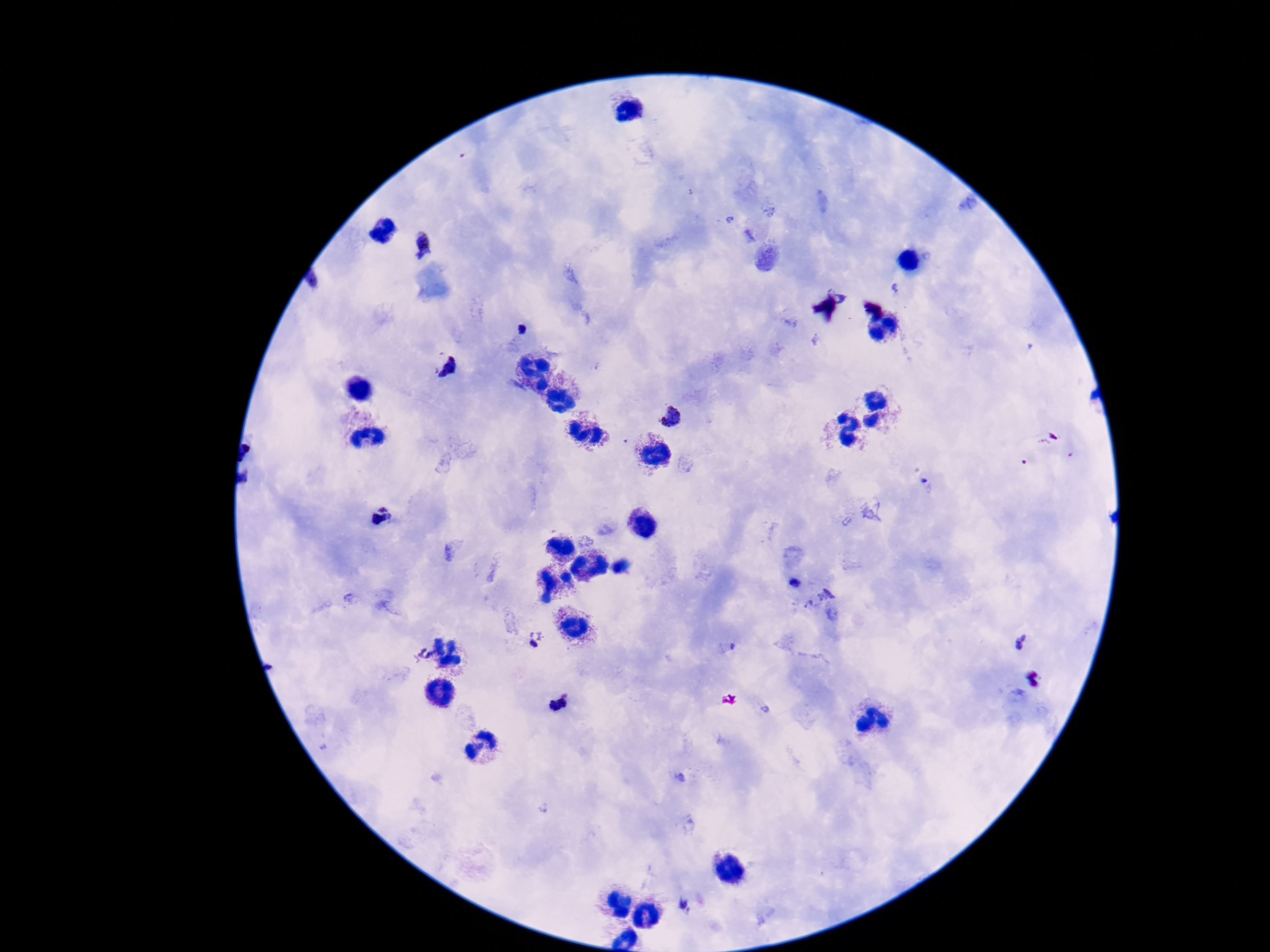

preparation: thick peripheral-blood smear
capture: smartphone camera through the microscope eyepiece
magnification: 100x
stain: Giemsa
image_size: 1270×952 pixels
field_of_view: one from this slide
plasmodium_parasite_locations: 'approximate object centers, in pixels from the top-left corner: (x=421, y=244), (x=446, y=366), (x=669, y=415), (x=382, y=515), (x=794, y=583), (x=535, y=641), (x=1021, y=641), (x=424, y=653), (x=559, y=703), (x=687, y=905)'
patient_malaria_status: positive